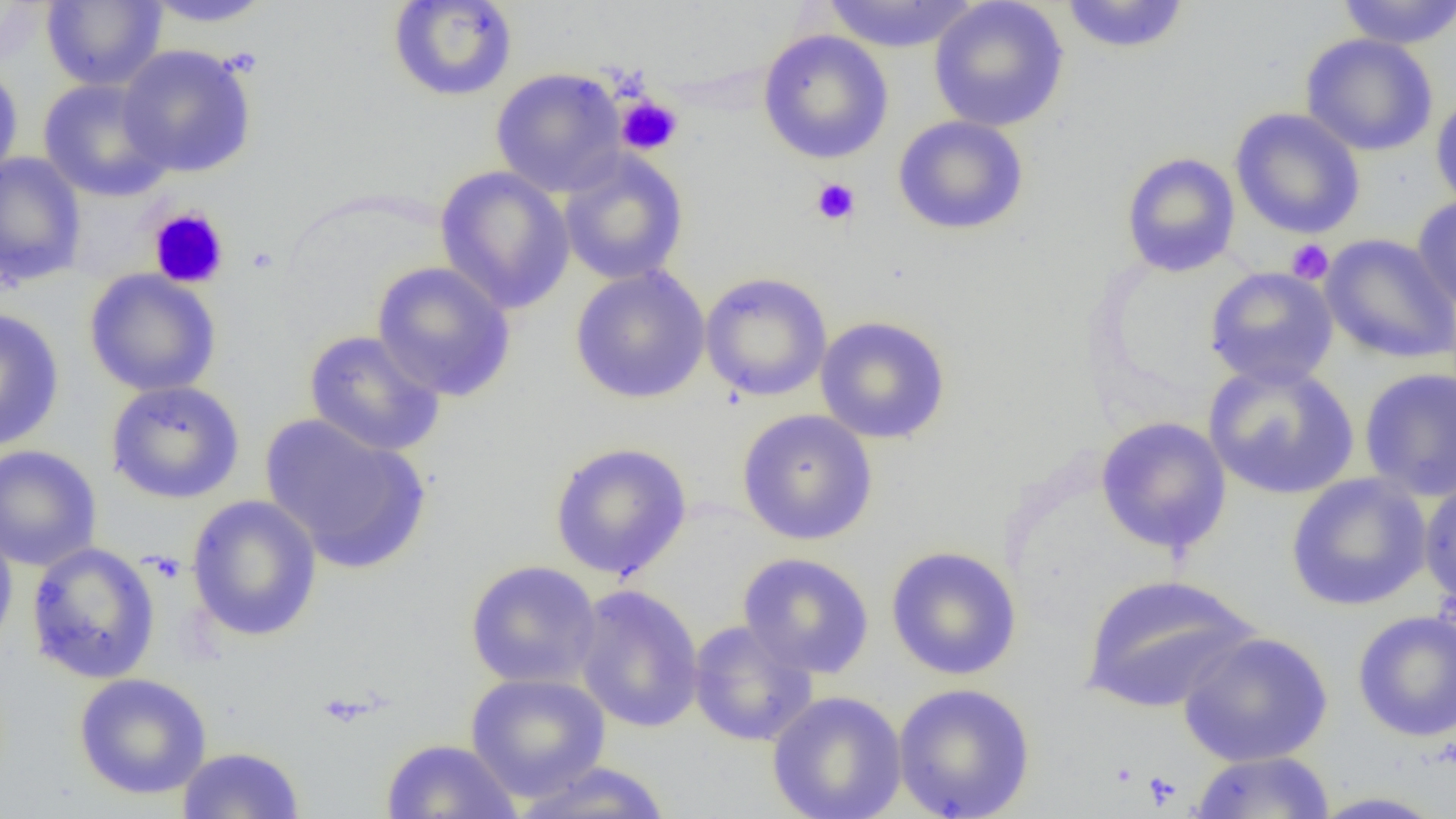
Summary:
  - Coordinate format: approximate bounding boxes as named x1/y1/x2/y2 corners in pixels
  - Uninfected red blood cell locations: (x1=142, y1=0, x2=277, y2=28), (x1=387, y1=0, x2=518, y2=102), (x1=820, y1=0, x2=979, y2=53), (x1=929, y1=0, x2=1069, y2=132), (x1=1059, y1=0, x2=1191, y2=55), (x1=1336, y1=0, x2=1455, y2=49), (x1=41, y1=1, x2=167, y2=90), (x1=758, y1=29, x2=894, y2=165), (x1=1300, y1=33, x2=1439, y2=157), (x1=117, y1=44, x2=257, y2=177), (x1=0, y1=61, x2=24, y2=188), (x1=490, y1=67, x2=628, y2=197), (x1=37, y1=78, x2=175, y2=202), (x1=1430, y1=89, x2=1456, y2=214), (x1=1229, y1=107, x2=1366, y2=240), (x1=892, y1=115, x2=1030, y2=236), (x1=557, y1=149, x2=690, y2=286), (x1=1121, y1=151, x2=1240, y2=277), (x1=0, y1=152, x2=87, y2=288), (x1=435, y1=166, x2=575, y2=315), (x1=1411, y1=195, x2=1456, y2=316), (x1=1320, y1=234, x2=1456, y2=364), (x1=371, y1=261, x2=517, y2=402), (x1=569, y1=265, x2=711, y2=405), (x1=1204, y1=266, x2=1339, y2=389), (x1=84, y1=269, x2=221, y2=397), (x1=700, y1=271, x2=832, y2=401), (x1=0, y1=307, x2=65, y2=450), (x1=814, y1=315, x2=951, y2=444), (x1=303, y1=329, x2=446, y2=457), (x1=1202, y1=361, x2=1359, y2=501), (x1=1359, y1=367, x2=1456, y2=502), (x1=105, y1=380, x2=245, y2=504), (x1=736, y1=409, x2=877, y2=545), (x1=260, y1=414, x2=430, y2=572), (x1=1095, y1=416, x2=1232, y2=557), (x1=549, y1=441, x2=692, y2=581), (x1=0, y1=445, x2=102, y2=572), (x1=1286, y1=472, x2=1433, y2=612), (x1=1419, y1=475, x2=1456, y2=610), (x1=185, y1=494, x2=323, y2=642), (x1=0, y1=520, x2=18, y2=656), (x1=25, y1=541, x2=162, y2=685), (x1=885, y1=545, x2=1022, y2=681), (x1=737, y1=552, x2=875, y2=678), (x1=465, y1=559, x2=602, y2=690), (x1=1080, y1=573, x2=1259, y2=713), (x1=573, y1=584, x2=704, y2=734), (x1=1352, y1=610, x2=1456, y2=742), (x1=688, y1=619, x2=819, y2=747), (x1=1176, y1=630, x2=1334, y2=767), (x1=465, y1=671, x2=611, y2=801), (x1=73, y1=672, x2=212, y2=799), (x1=892, y1=682, x2=1036, y2=819), (x1=767, y1=690, x2=907, y2=819), (x1=380, y1=738, x2=522, y2=819), (x1=177, y1=745, x2=305, y2=818), (x1=1189, y1=751, x2=1336, y2=818), (x1=510, y1=761, x2=674, y2=818), (x1=1307, y1=790, x2=1452, y2=818)
  - Platelet locations: (x1=615, y1=95, x2=683, y2=157), (x1=811, y1=177, x2=861, y2=225), (x1=147, y1=206, x2=229, y2=289), (x1=1286, y1=238, x2=1334, y2=284), (x1=1142, y1=771, x2=1182, y2=809)
  - Slide-level diagnosis: negative for blood parasites
  - Image size: 1456×819 pixels
  - Modality: optical microscopy
  - Magnification: 1000x
  - Field of view: one of a larger specimen
  - Preparation: thin blood film